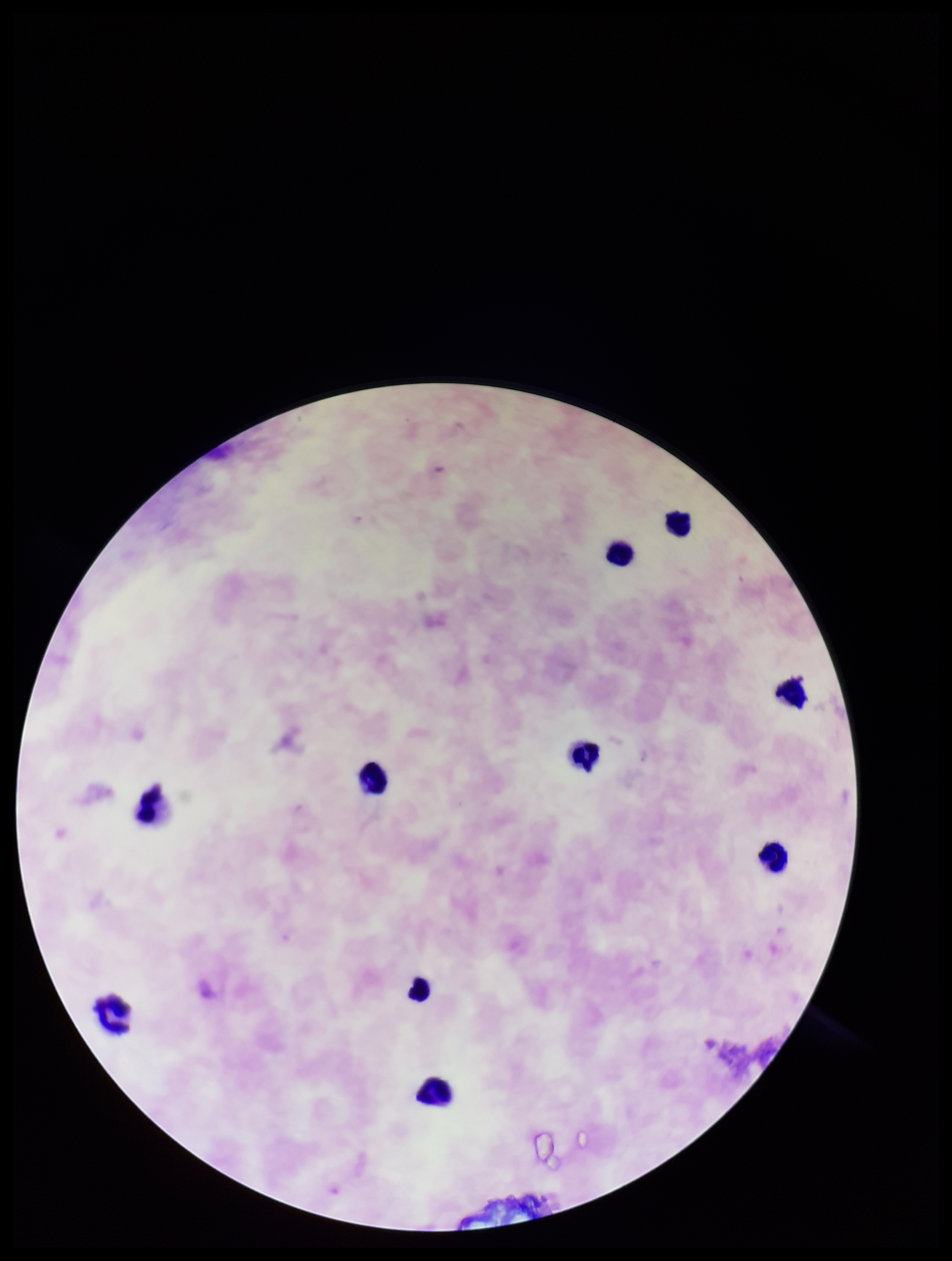
{
  "leukocyte_count": 10,
  "plasmodium_parasites": "none seen",
  "image_size": "952×1261 pixels",
  "capture": "smartphone photograph through the microscope eyepiece",
  "species_reported_for_this_patient": "Plasmodium falciparum",
  "stain": "Giemsa",
  "parasite_count": 0,
  "preparation": "thick",
  "patient_malaria_status": "positive",
  "field_of_view": "single"
}